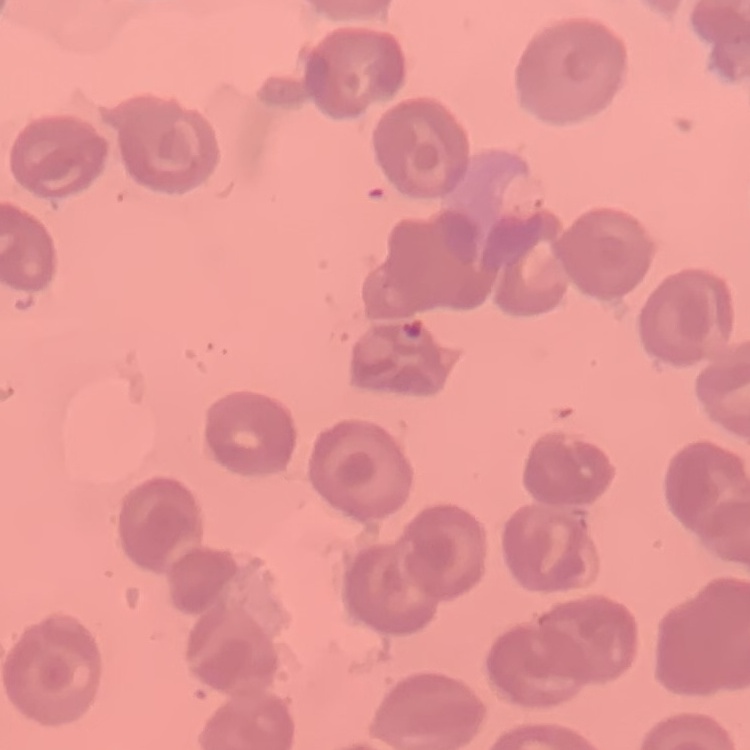 The erythrocytes show no rouleaux formation. Thin blood film. Square crop of a larger photomicrograph. Stained with either Field's or Giemsa.